Classify this cell by malaria status.
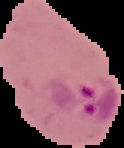
Parasitized.

image type = segmented cell region on a black background
image size = 124×148 pixels
preparation = thin blood film